Locate every leukocyte (white blood cell).
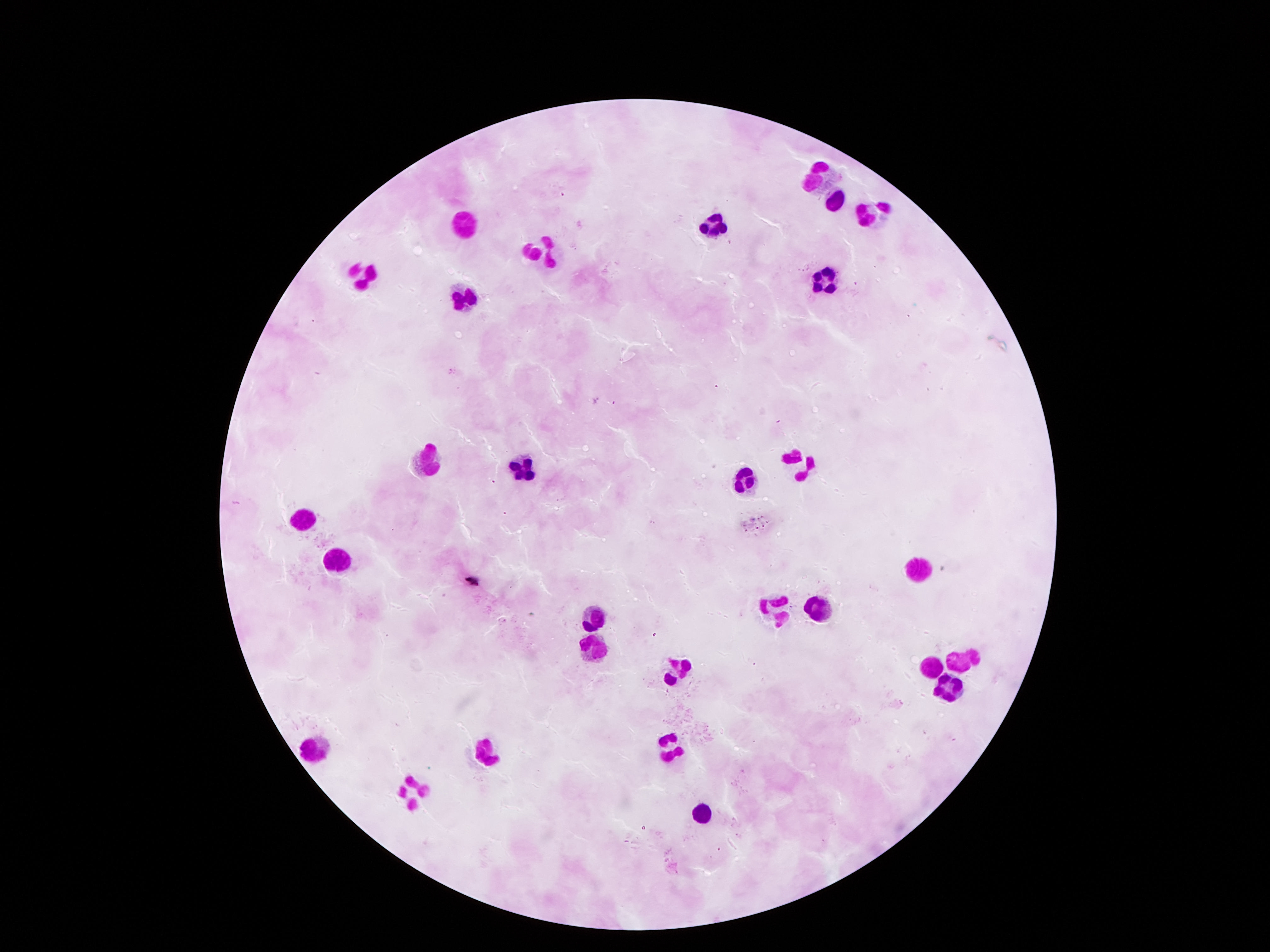

Approximate object centers, in pixels from the top-left corner.
Leukocytes: (x=822, y=174), (x=836, y=204), (x=873, y=211), (x=462, y=225), (x=715, y=225), (x=543, y=248), (x=361, y=268), (x=823, y=276), (x=465, y=300), (x=428, y=457), (x=800, y=462), (x=524, y=468), (x=745, y=478), (x=305, y=517), (x=332, y=557), (x=919, y=575), (x=779, y=603), (x=819, y=605), (x=594, y=612), (x=592, y=645), (x=962, y=660), (x=680, y=666), (x=929, y=666), (x=946, y=687), (x=314, y=743), (x=675, y=747), (x=488, y=752), (x=410, y=793), (x=701, y=811).

Smartphone photograph taken through the microscope eyepiece. Image is 1270×952 pixels. Giemsa-stained preparation. 100x magnification. Patient malaria status: negative. Single field of view. Thick blood smear.